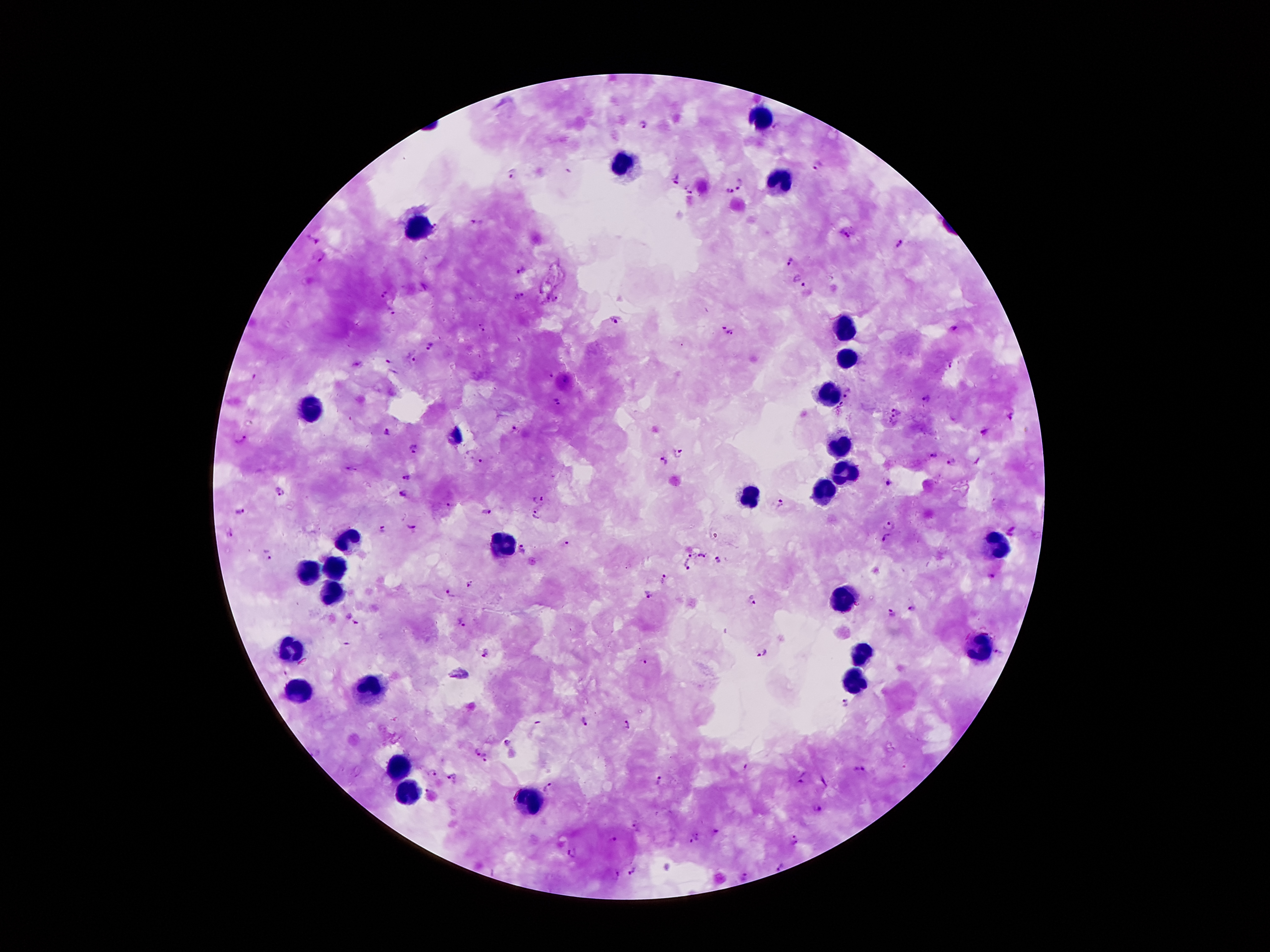
Approximate centers as [x, y] in pixels.
Summary:
  - Leukocyte locations: [760, 117], [621, 165], [779, 182], [415, 225], [844, 330], [847, 354], [832, 391], [312, 410], [840, 448], [847, 474], [823, 491], [751, 496], [350, 542], [508, 544], [991, 547], [331, 570], [309, 575], [331, 592], [842, 601], [976, 649], [290, 650], [864, 655], [849, 683], [297, 686], [369, 688], [401, 767], [410, 796], [525, 801]
  - Malaria parasite locations: [644, 126], [776, 126], [819, 166], [512, 174], [674, 180], [742, 185], [686, 190], [728, 191], [478, 221], [848, 233], [313, 240], [902, 245], [320, 257], [790, 262], [521, 268], [799, 282], [386, 294], [520, 296], [556, 298], [392, 313], [615, 322], [482, 327], [954, 327], [730, 334], [431, 346], [388, 361], [414, 361], [552, 375], [566, 380], [850, 394], [928, 400], [560, 402], [842, 406], [898, 410], [1010, 417], [894, 422], [387, 432], [515, 432], [986, 432], [240, 437], [414, 450], [680, 451], [934, 456], [662, 461], [952, 461], [480, 462], [407, 477], [889, 485], [280, 490], [402, 494], [541, 497], [782, 503], [450, 505], [239, 510], [487, 512], [536, 517], [891, 523], [410, 524], [380, 530], [229, 532], [886, 539], [566, 545], [523, 550], [692, 553], [267, 556], [702, 556], [719, 560], [687, 567], [995, 576], [665, 580], [471, 584], [451, 593], [649, 593], [753, 602], [911, 608], [892, 613], [357, 621], [459, 623], [763, 652], [998, 652], [487, 653], [647, 662], [845, 705], [584, 722], [628, 726], [505, 743], [477, 751], [484, 758], [861, 770], [435, 772], [454, 776], [803, 779], [660, 782], [550, 787], [428, 790], [816, 810], [635, 824], [715, 832], [697, 835], [616, 838], [795, 838], [572, 854], [780, 866], [634, 869], [614, 875], [746, 876]
  - Field of view: one from this slide
  - Preparation: thick blood smear
  - Image size: 1270×952 pixels
  - Patient malaria status: infected with Plasmodium falciparum
  - Stain: Giemsa
  - Capture: smartphone through the microscope eyepiece
  - Magnification: 100x